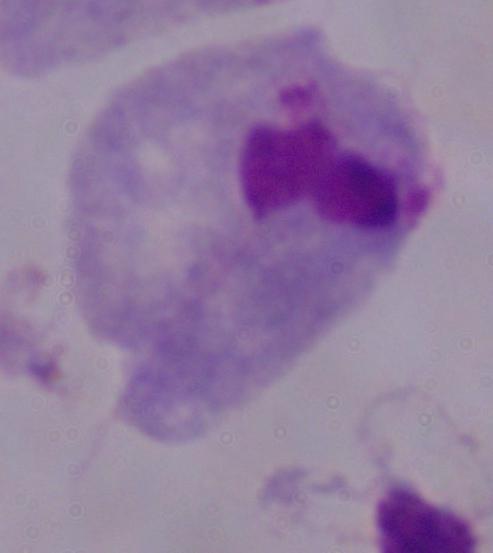 Photomicrograph. A trichomonad is seen. 1000x magnification.